Locate every white blood cell.
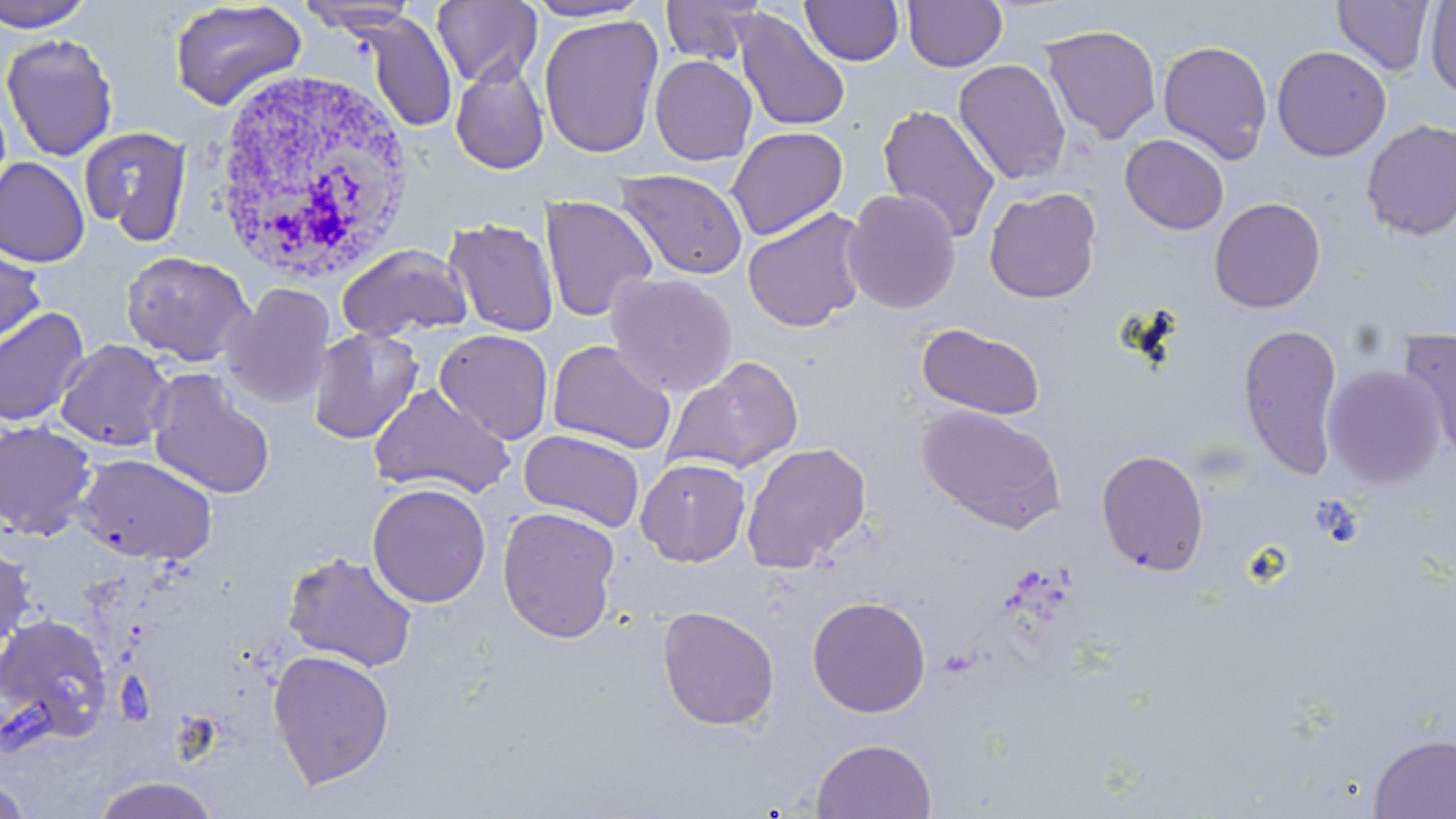
Approximate bounding boxes as (x1, y1, x2, y2) in pixels.
White blood cells: (210, 66, 415, 282).

Summary:
  - Uninfected red blood cell locations: (0, 0, 98, 33), (658, 0, 764, 66), (800, 0, 904, 66), (902, 0, 1007, 73), (1332, 0, 1435, 76), (167, 1, 308, 113), (296, 1, 422, 34), (432, 1, 542, 87), (524, 1, 651, 23), (1425, 1, 1456, 101), (734, 10, 851, 133), (919, 11, 1034, 114), (362, 13, 457, 134), (539, 14, 664, 159), (1039, 24, 1162, 144), (1, 32, 119, 162), (1156, 40, 1274, 164), (1271, 45, 1392, 161), (649, 55, 757, 165), (953, 58, 1071, 185), (450, 59, 550, 175), (877, 104, 1001, 243), (1360, 118, 1456, 241), (79, 126, 193, 244), (726, 126, 848, 241), (1120, 133, 1229, 235), (0, 157, 90, 267), (612, 167, 749, 281), (983, 186, 1102, 304), (842, 189, 961, 314), (540, 195, 657, 322), (1208, 197, 1326, 313), (741, 207, 870, 333), (443, 217, 559, 338), (0, 239, 46, 352), (335, 244, 473, 343), (120, 250, 256, 367), (604, 272, 738, 397), (222, 282, 336, 409), (0, 307, 91, 426), (917, 322, 1046, 420), (1237, 322, 1343, 480), (308, 327, 424, 444), (433, 328, 554, 445), (1397, 329, 1456, 467), (54, 338, 175, 452), (547, 339, 676, 455), (662, 355, 805, 477), (1322, 365, 1445, 487), (146, 371, 276, 500), (367, 383, 515, 500), (918, 404, 1066, 534), (0, 419, 98, 540), (518, 430, 646, 531), (740, 441, 872, 573), (1096, 448, 1209, 576), (74, 452, 218, 566), (635, 458, 751, 567), (366, 482, 492, 608), (497, 507, 621, 644), (0, 540, 36, 651), (281, 550, 418, 672), (807, 595, 931, 718), (657, 604, 780, 731), (0, 612, 115, 747), (267, 649, 395, 789), (1368, 733, 1456, 818), (811, 737, 938, 818), (0, 775, 36, 818), (88, 775, 225, 818)
  - Slide-level diagnosis: Plasmodium ovale
  - Preparation: thin blood smear
  - Magnification: 1000x
  - Modality: light microscopy
  - Field of view: single
  - Stain: May-Grünwald-Giemsa
  - Image size: 1456×819 pixels